Report the malaria status of this cell.
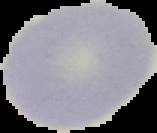
Uninfected.

preparation: thin blood film
image_type: segmented cell region on a black background
image_size: 157×133 pixels